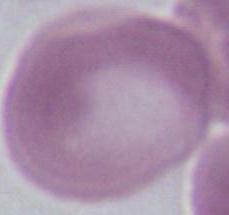
A red blood cell is shown. Captured at 1000x magnification. Photomicrograph.